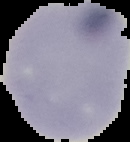
image_type: cell region segmented out of the field of view; surrounding area masked to black
image_size: 130×142 pixels
malaria_status: uninfected
preparation: thin blood smear